Identify the cell.
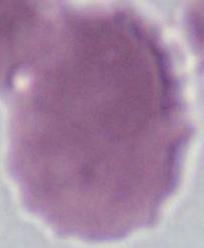

This is an erythrocyte.

Summary:
  - Magnification: 1000x
  - Modality: photomicrograph